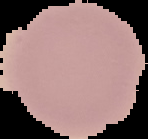
Malaria status: uninfected. Image is 148×139 pixels. From a thin blood film. Segmented cell region on a black background.